Name the cell type shown.
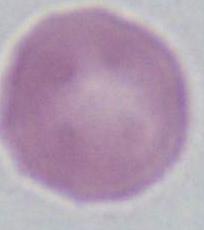
This is an erythrocyte.

Captured at 1000x magnification. Micrograph.